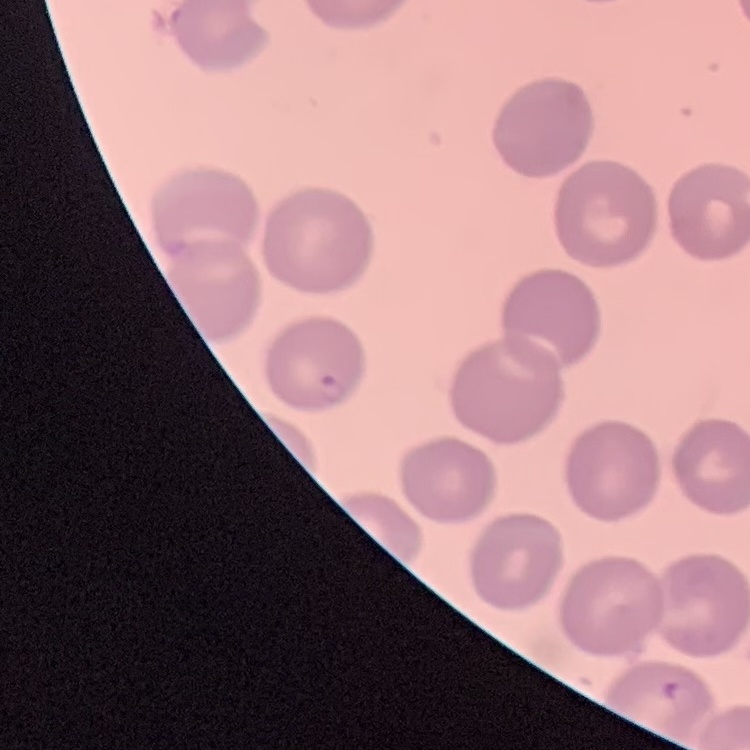

The red blood cells show no rouleaux formation. Stained with either Field's or Giemsa. Square crop of a larger photomicrograph. Thin peripheral smear.